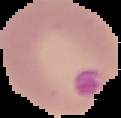

Summary:
  - Image type: cell region segmented out of the field of view; surrounding area masked to black
  - Image size: 121×118 pixels
  - Preparation: thin blood smear
  - Result: malaria parasites identified